Point out each Plasmodium parasite.
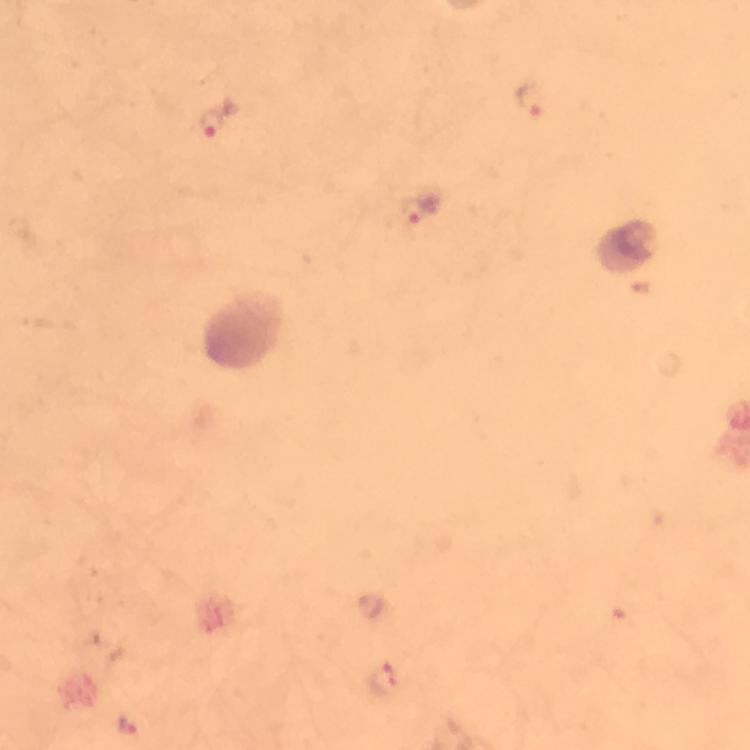
Approximate centers as {x, y} in pixels.
Plasmodium parasites: {534, 105}, {214, 127}, {416, 213}, {387, 680}, {127, 727}.

Photographed through the microscope with a smartphone camera. A crop from one field of view. Immersion oil was used. 100x magnification. Thick smear. Image is 750×750 pixels. From a malaria diagnostic workup. Giemsa stain.